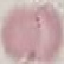
malaria status = uninfected
preparation = thin blood film
capture = smartphone through the microscope eyepiece
stain = Giemsa
image type = automatically extracted cell patch, resized to 64 × 64 pixels